Locate every blood parasite and identify its species.
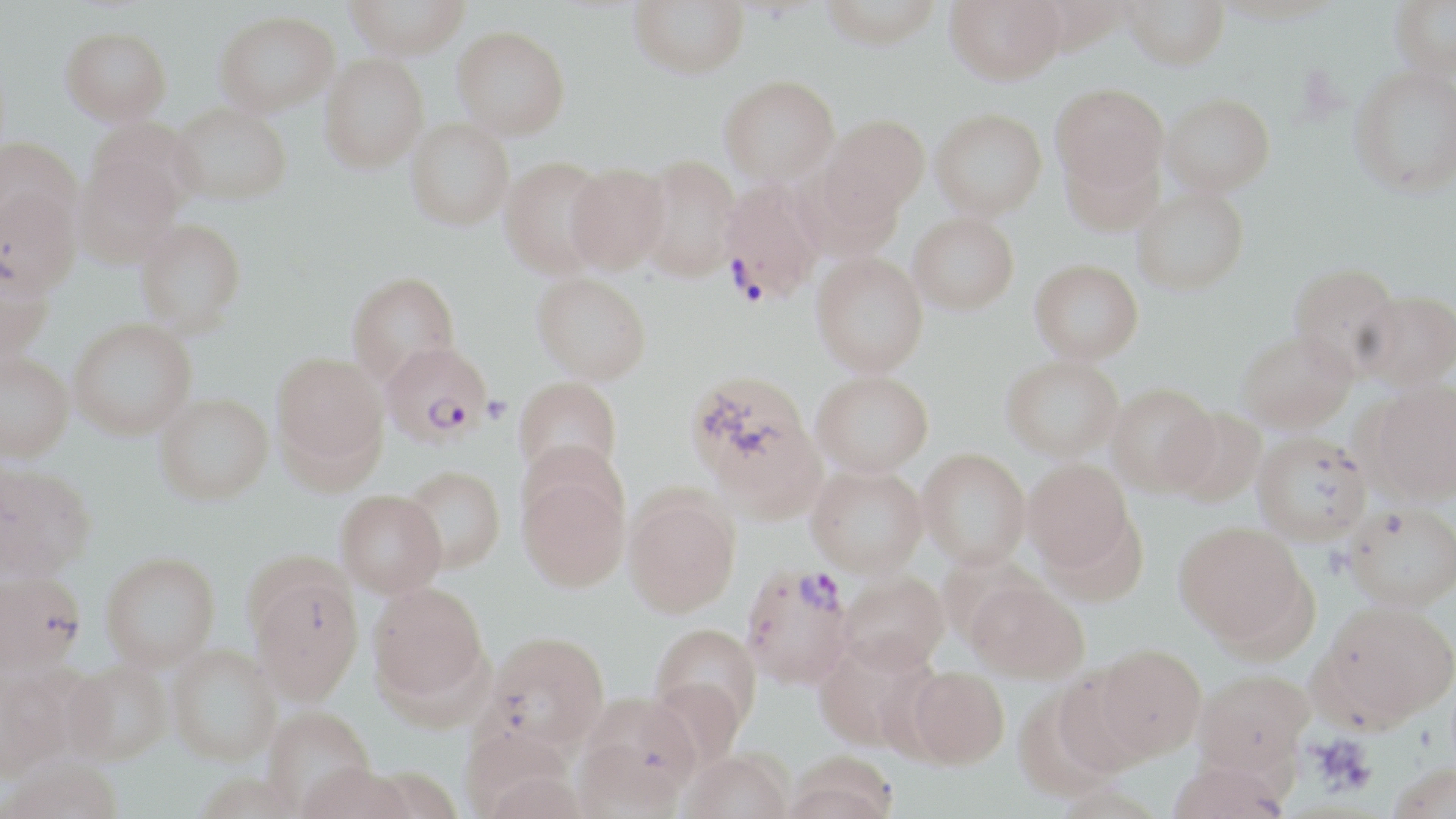
Approximate bounding boxes as named x1/y1/x2/y2 corners in pixels.
Plasmodium falciparum-infected red blood cells: (x1=718, y1=180, x2=825, y2=304), (x1=380, y1=341, x2=492, y2=445), (x1=739, y1=562, x2=853, y2=690).
No Plasmodium ovale, Plasmodium malariae, Plasmodium vivax, Babesia divergens, or Trypanosoma brucei observed.

Platelet locations: (x1=482, y1=396, x2=511, y2=423), (x1=1309, y1=733, x2=1376, y2=795). Uninfected red blood cell locations: (x1=343, y1=0, x2=472, y2=58), (x1=629, y1=0, x2=748, y2=77), (x1=817, y1=0, x2=944, y2=48), (x1=946, y1=0, x2=1066, y2=83), (x1=1122, y1=0, x2=1230, y2=69), (x1=1390, y1=1, x2=1456, y2=84), (x1=214, y1=10, x2=339, y2=114), (x1=452, y1=26, x2=570, y2=139), (x1=60, y1=27, x2=172, y2=126), (x1=320, y1=54, x2=428, y2=172), (x1=1349, y1=67, x2=1456, y2=198), (x1=720, y1=75, x2=840, y2=184), (x1=1051, y1=83, x2=1169, y2=198), (x1=1161, y1=94, x2=1275, y2=197), (x1=170, y1=103, x2=292, y2=204), (x1=930, y1=107, x2=1047, y2=221), (x1=820, y1=114, x2=930, y2=223), (x1=85, y1=116, x2=199, y2=224), (x1=406, y1=117, x2=514, y2=230), (x1=0, y1=136, x2=82, y2=237), (x1=1060, y1=143, x2=1164, y2=237), (x1=74, y1=154, x2=182, y2=268), (x1=637, y1=154, x2=743, y2=282), (x1=499, y1=156, x2=611, y2=279), (x1=565, y1=163, x2=670, y2=273), (x1=0, y1=186, x2=81, y2=299), (x1=1133, y1=187, x2=1249, y2=294), (x1=908, y1=212, x2=1019, y2=314), (x1=136, y1=219, x2=246, y2=332), (x1=811, y1=252, x2=928, y2=376), (x1=0, y1=257, x2=54, y2=363), (x1=1029, y1=259, x2=1143, y2=363), (x1=1289, y1=262, x2=1401, y2=372), (x1=347, y1=271, x2=461, y2=386), (x1=532, y1=273, x2=652, y2=384), (x1=1355, y1=289, x2=1456, y2=389), (x1=68, y1=319, x2=196, y2=438), (x1=1237, y1=330, x2=1355, y2=432), (x1=0, y1=351, x2=74, y2=460), (x1=272, y1=351, x2=388, y2=472), (x1=1001, y1=355, x2=1124, y2=461), (x1=811, y1=370, x2=933, y2=476), (x1=685, y1=371, x2=821, y2=507), (x1=514, y1=376, x2=622, y2=482), (x1=1366, y1=381, x2=1456, y2=503), (x1=1106, y1=382, x2=1219, y2=495), (x1=154, y1=394, x2=273, y2=504), (x1=1167, y1=408, x2=1267, y2=508), (x1=1252, y1=432, x2=1372, y2=544), (x1=516, y1=437, x2=629, y2=532), (x1=918, y1=448, x2=1031, y2=568), (x1=1022, y1=458, x2=1133, y2=574), (x1=0, y1=462, x2=96, y2=581), (x1=806, y1=464, x2=928, y2=577), (x1=401, y1=465, x2=506, y2=573), (x1=517, y1=471, x2=630, y2=592), (x1=336, y1=489, x2=447, y2=596), (x1=624, y1=491, x2=740, y2=617), (x1=1343, y1=503, x2=1456, y2=610), (x1=1174, y1=521, x2=1310, y2=648), (x1=101, y1=552, x2=220, y2=670), (x1=249, y1=569, x2=364, y2=704), (x1=0, y1=571, x2=87, y2=675), (x1=840, y1=571, x2=948, y2=672), (x1=967, y1=580, x2=1089, y2=683), (x1=367, y1=581, x2=489, y2=709), (x1=1319, y1=601, x2=1456, y2=726), (x1=650, y1=622, x2=762, y2=734), (x1=483, y1=631, x2=610, y2=753), (x1=814, y1=635, x2=940, y2=754), (x1=1095, y1=643, x2=1206, y2=758), (x1=168, y1=645, x2=280, y2=765), (x1=61, y1=660, x2=172, y2=764), (x1=905, y1=665, x2=1009, y2=768), (x1=0, y1=667, x2=71, y2=779), (x1=1194, y1=668, x2=1314, y2=776), (x1=1050, y1=671, x2=1154, y2=780), (x1=647, y1=676, x2=747, y2=772), (x1=1012, y1=683, x2=1126, y2=802), (x1=577, y1=691, x2=701, y2=811), (x1=263, y1=706, x2=375, y2=813), (x1=681, y1=750, x2=794, y2=819), (x1=784, y1=751, x2=900, y2=819), (x1=1, y1=758, x2=124, y2=819), (x1=1166, y1=758, x2=1290, y2=819), (x1=297, y1=763, x2=417, y2=819), (x1=1387, y1=763, x2=1455, y2=818). Slide-level diagnosis: Plasmodium falciparum. May-Grünwald-Giemsa stain. Optical microscopy. Thin blood smear. Captured at 1000x magnification. Single field of view. Image is 1456×819 pixels.